Classify this cell by malaria status.
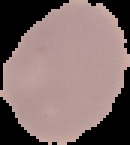
Uninfected.

image type = segmented cell region on a black background
preparation = thin blood film
image size = 130×145 pixels